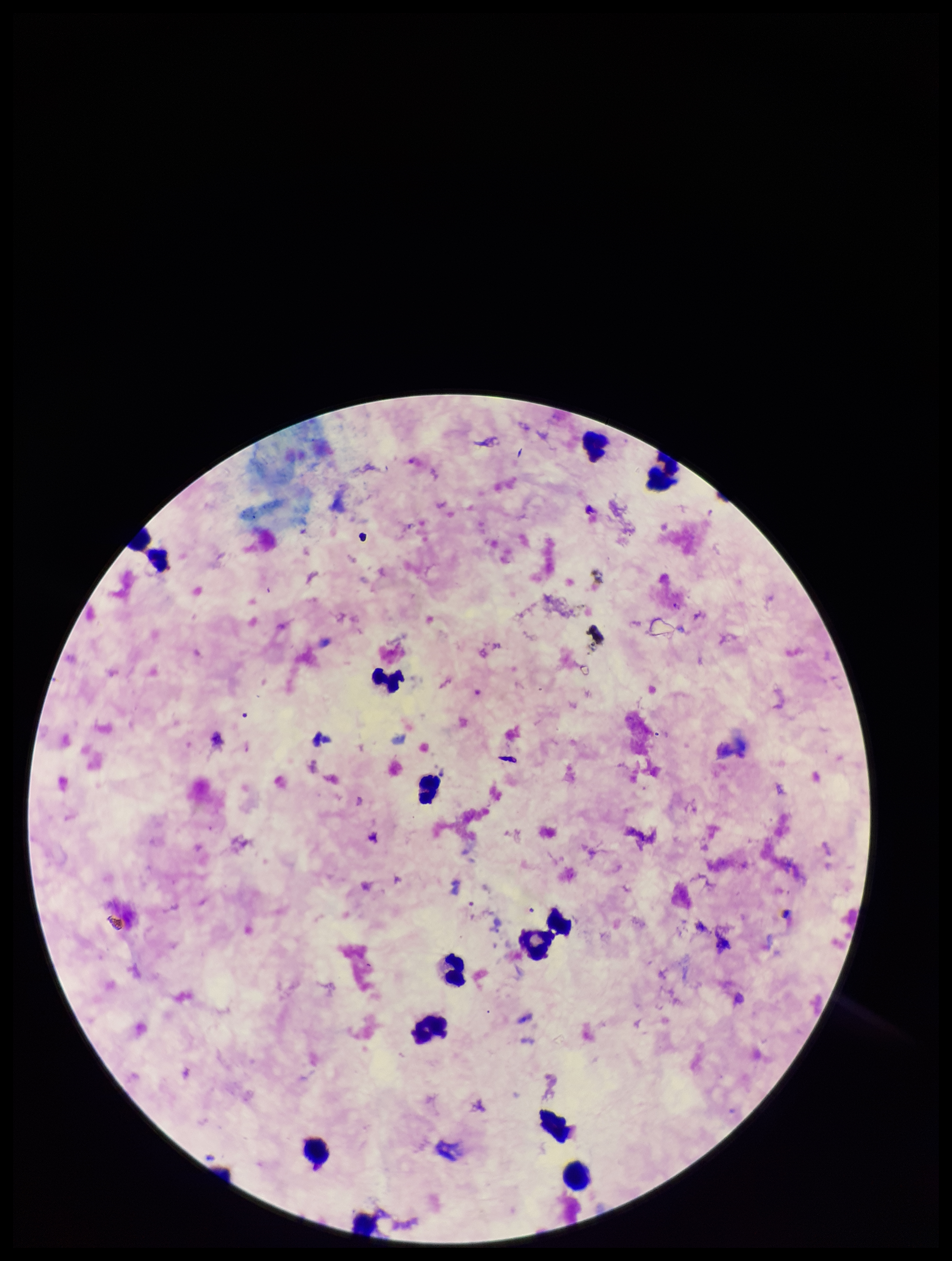

Plasmodium parasites = none detected
leukocyte count = 14
species reported for this patient = Plasmodium falciparum
image size = 952×1261 pixels
parasite count = 0
preparation = thick smear
field of view = single
capture = smartphone photograph through the microscope eyepiece
stain = Giemsa
patient malaria status = infected